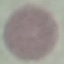

Malaria status: uninfected. Automatically extracted cell patch, resized to 64 × 64 pixels. Photographed with a smartphone camera at the microscope eyepiece. Thin blood smear. Giemsa-stained preparation.